Describe the morphology of the erythrocytes.
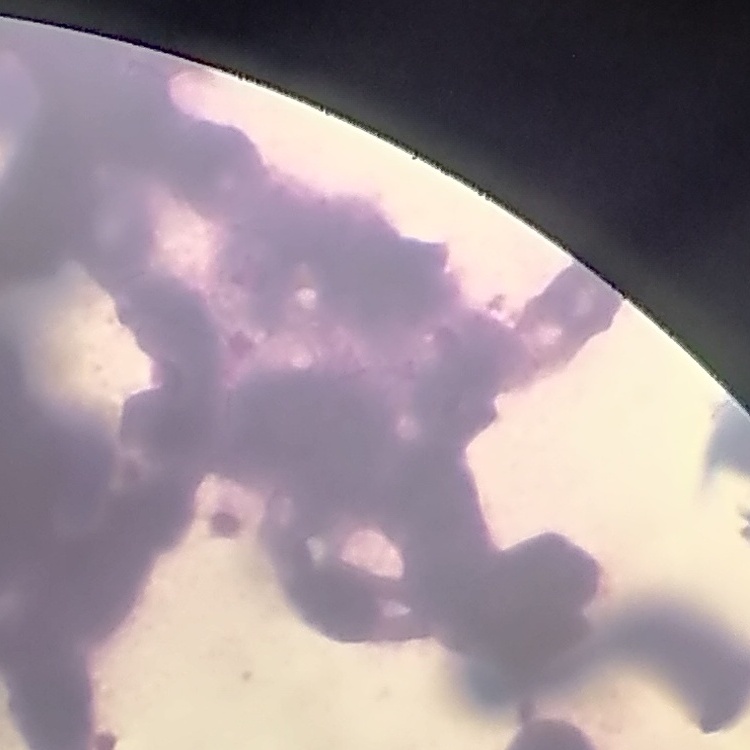
Rouleaux formation.

{
  "preparation": "thin blood smear",
  "image_type": "square crop of a larger photomicrograph",
  "stain": "Field's or Giemsa"
}